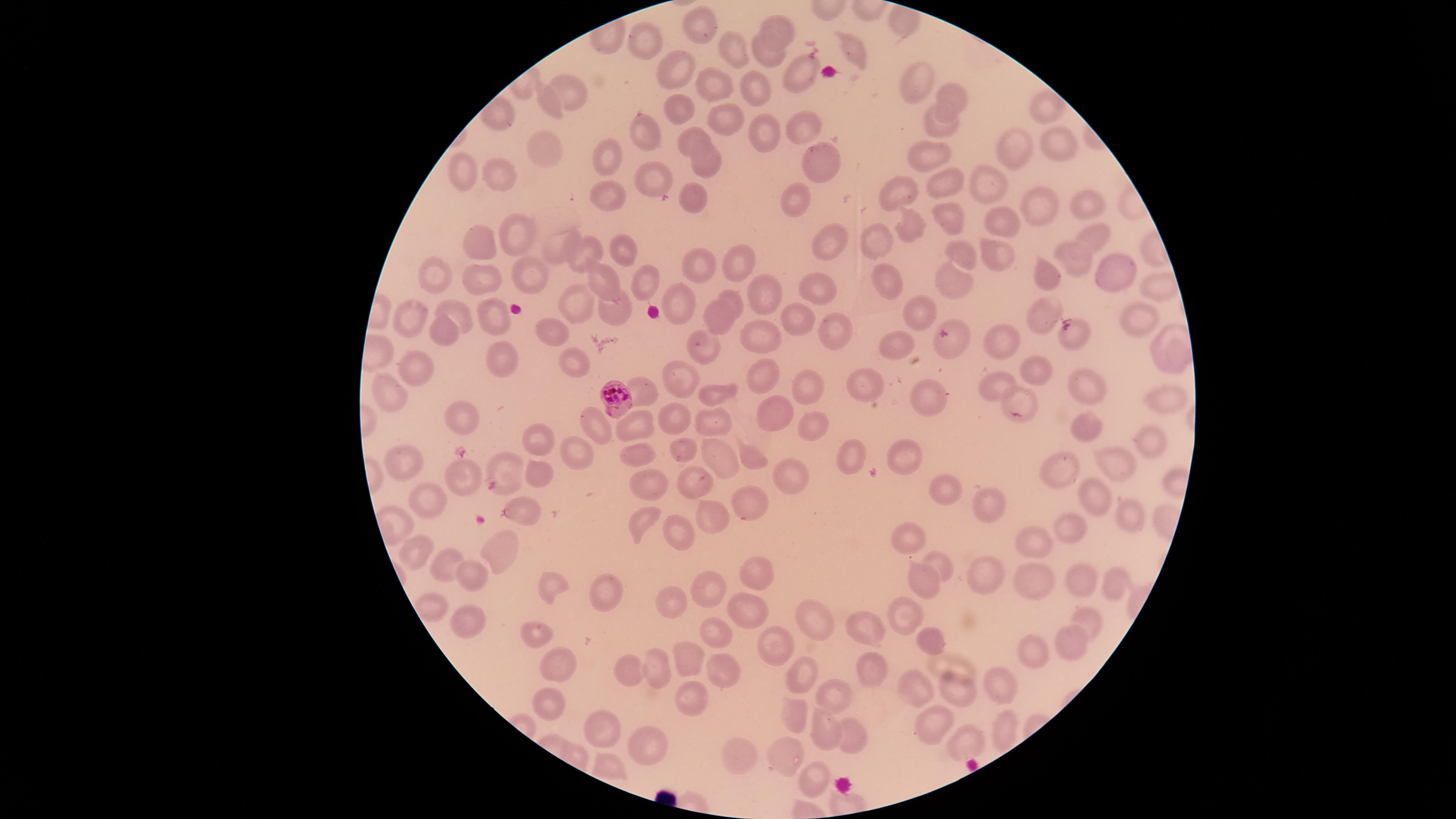 Approximate marker points as [x, y] in pixels. Parasitized red blood cells: [611, 396]. Uninfected red blood cells: [700, 27], [776, 29], [850, 47], [727, 50], [764, 60], [675, 70], [798, 76], [919, 80], [715, 88], [756, 88], [567, 89], [954, 95], [547, 104], [677, 107], [1044, 109], [721, 118], [803, 126], [938, 127], [760, 128], [648, 133], [693, 135], [1054, 143], [544, 147], [1019, 149], [927, 155], [608, 156], [706, 161], [820, 161], [499, 174], [467, 177], [947, 182], [656, 183], [986, 184], [912, 192], [685, 195], [609, 197], [800, 202], [1036, 205], [1088, 206], [951, 221], [516, 223], [1005, 223], [914, 231], [1093, 237], [478, 238], [831, 241], [875, 241], [557, 245], [621, 249], [587, 250], [964, 251], [1000, 258], [1067, 260], [692, 265], [739, 266], [521, 267], [1109, 269], [436, 272], [1051, 272], [479, 274], [956, 276], [600, 278], [888, 280], [645, 282], [818, 286], [764, 295], [729, 297], [679, 298], [580, 302], [618, 309], [920, 309], [1043, 311], [461, 313], [719, 315], [1132, 316], [493, 317], [795, 317], [411, 320], [554, 329], [1075, 330], [835, 331], [439, 332], [761, 334], [997, 337], [952, 338], [705, 346], [901, 347], [496, 357], [574, 359], [415, 362], [759, 372], [1039, 375], [684, 380], [868, 386], [1000, 386], [641, 388], [810, 389], [1088, 389], [719, 392], [393, 395], [929, 397], [1020, 399], [1158, 402], [775, 411], [670, 414], [463, 415], [710, 416], [635, 418], [589, 420], [1083, 422], [814, 424], [1152, 439], [536, 441], [682, 448], [905, 449], [852, 451], [578, 452], [637, 453], [751, 457], [506, 459], [1124, 459], [401, 460], [717, 461], [1071, 467], [788, 476], [465, 478], [539, 482], [689, 482], [651, 484], [944, 487], [1102, 493], [515, 503], [753, 504], [988, 504], [429, 505], [1127, 509], [709, 512], [639, 521], [1070, 524], [911, 532], [675, 533], [1039, 543], [415, 546], [496, 548], [449, 560], [936, 562], [759, 571], [976, 572], [475, 573], [1028, 573], [1079, 573], [921, 582], [1110, 584], [552, 587], [710, 592], [601, 593], [675, 602], [905, 606], [424, 607], [752, 612], [1087, 617], [810, 618], [468, 622], [535, 626], [710, 631], [870, 631], [928, 636], [1067, 643], [774, 644], [1036, 655], [689, 661], [555, 662], [651, 667], [718, 669], [630, 671], [808, 675], [872, 675], [916, 684], [948, 687], [1000, 688], [545, 698], [690, 698], [829, 700], [796, 707], [997, 722], [822, 728], [931, 728], [604, 729], [849, 739], [965, 739], [643, 749], [743, 755], [781, 756], [606, 767], [812, 774]. Thin blood film. Presence: malaria parasites seen. Giemsa-stained preparation. The visible region is circular. Single field of view. Image is 1456×819 pixels. Photographed with a smartphone camera through the microscope eyepiece. Species: Plasmodium falciparum.